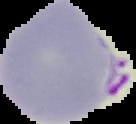
Summary:
  - Result: Plasmodium parasites detected
  - Image type: segmented cell region with the area outside set to black
  - Image size: 136×124 pixels
  - Preparation: thin blood film